Report the malaria status of this cell.
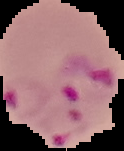

Parasitized.

Summary:
  - Image size: 124×151 pixels
  - Preparation: thin blood film
  - Image type: segmented cell region on a black background